Locate every uninfected red blood cell.
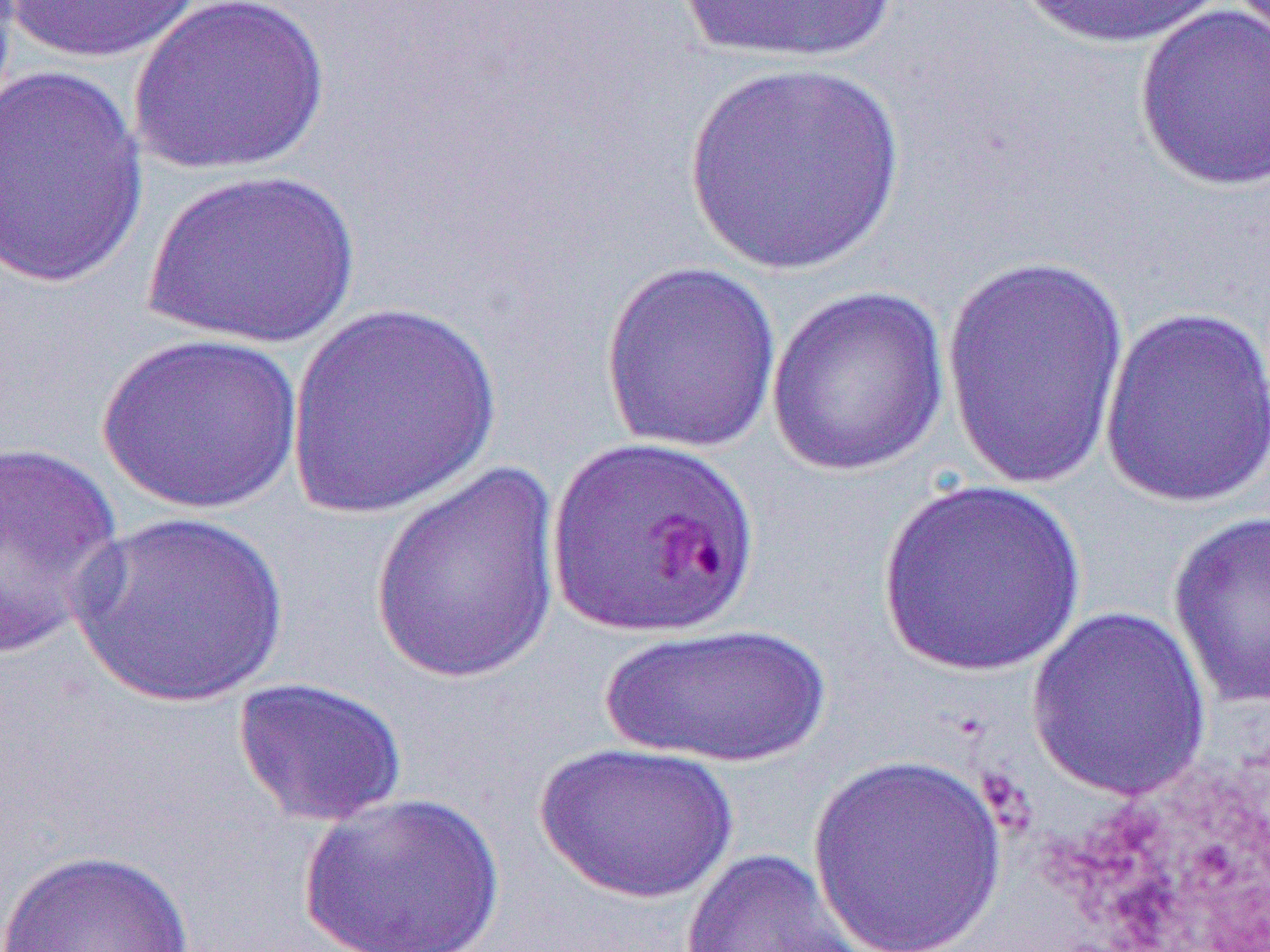
Approximate bounding boxes as [x1, y1, x2, y2] in pixels.
Uninfected red blood cells: [4, 0, 208, 64], [130, 0, 332, 176], [669, 0, 905, 67], [1009, 0, 1237, 51], [1134, 4, 1269, 193], [682, 63, 908, 278], [1, 65, 149, 290], [143, 168, 361, 349], [941, 255, 1132, 493], [599, 261, 783, 454], [766, 285, 948, 478], [285, 302, 503, 519], [1099, 305, 1270, 509], [95, 332, 304, 515], [0, 440, 127, 661], [369, 459, 565, 690], [875, 477, 1086, 677], [1167, 511, 1269, 709], [69, 512, 292, 709], [1026, 605, 1212, 802], [598, 623, 833, 769], [232, 676, 408, 828], [532, 741, 740, 905], [807, 751, 1009, 950], [297, 789, 506, 952], [0, 847, 198, 951], [678, 847, 881, 951].

Slide-level diagnosis: Plasmodium falciparum. Thin blood smear. Light microscopy. Single field of view. Captured at 1000x magnification. Image is 1270×952 pixels.